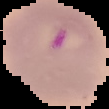

Summary:
  - Image type: segmented cell region on a black background
  - Malaria status: parasitized
  - Preparation: thin blood smear
  - Image size: 109×109 pixels